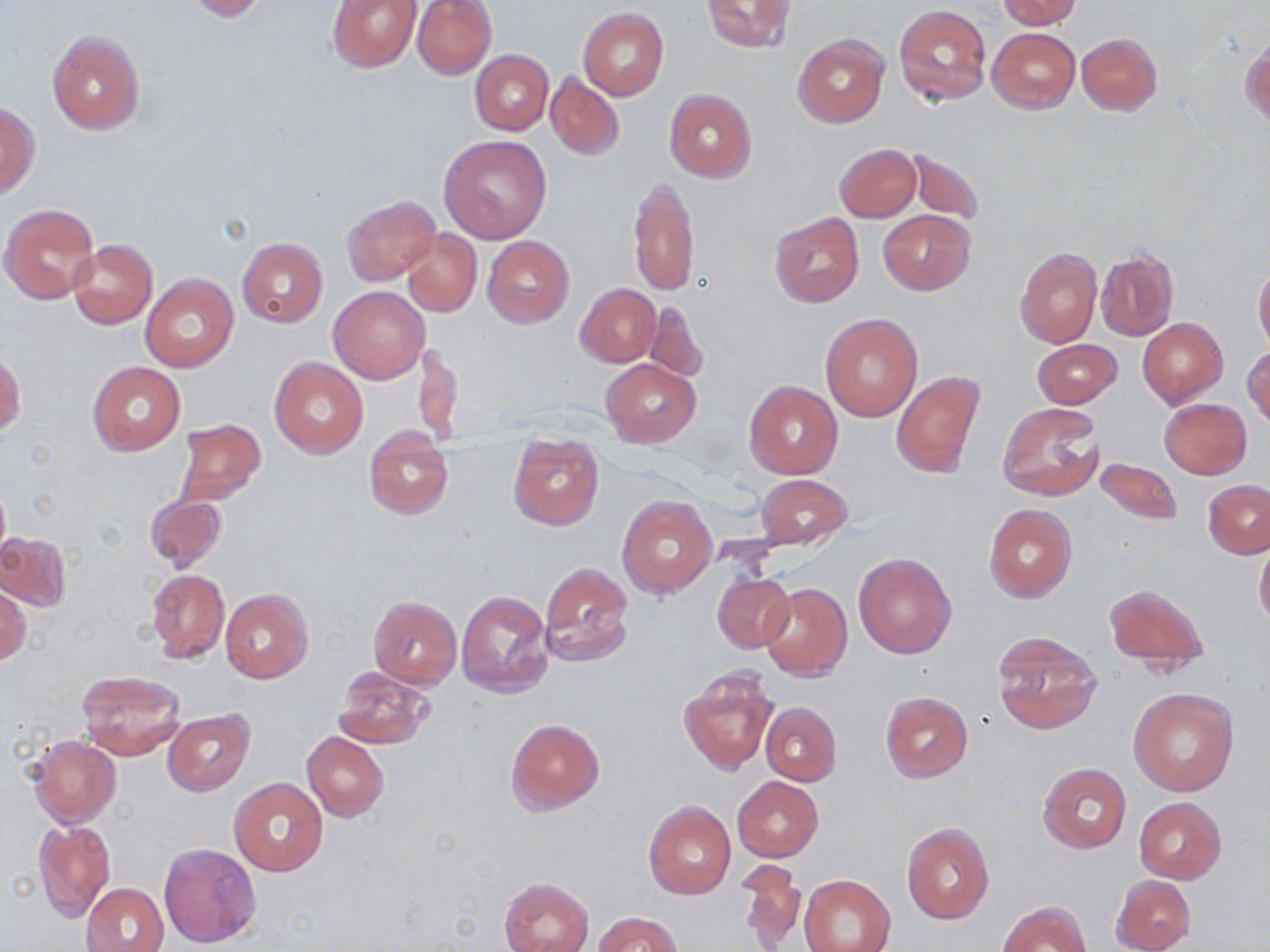

slide_level_diagnosis: negative for blood parasites
modality: optical microscopy
preparation: thin blood film
field_of_view: single
stain: May-Grünwald-Giemsa
magnification: 1000x
image_size: 1270×952 pixels
uninfected_red_blood_cell_locations: 'approximate bounding boxes as (x1, y1, x2, y2) in pixels: (182, 0, 267, 21), (328, 0, 421, 73), (412, 0, 496, 79), (998, 0, 1083, 28), (700, 1, 796, 54), (894, 5, 991, 106), (577, 8, 668, 100), (988, 27, 1080, 114), (47, 30, 144, 135), (1076, 33, 1162, 115), (1241, 34, 1269, 131), (793, 35, 888, 127), (471, 50, 552, 134), (544, 71, 624, 162), (664, 88, 757, 184), (0, 100, 38, 197), (440, 135, 552, 243), (834, 143, 921, 223), (904, 148, 985, 227), (629, 174, 700, 297), (342, 194, 441, 286), (1, 203, 99, 303), (769, 210, 865, 308), (878, 211, 975, 294), (400, 228, 482, 317), (482, 236, 574, 327), (236, 238, 328, 328), (67, 239, 158, 330), (1014, 248, 1101, 348), (1095, 249, 1180, 342), (1254, 259, 1270, 354), (141, 274, 237, 372), (575, 283, 660, 367), (329, 287, 429, 384), (643, 299, 709, 384), (821, 313, 923, 421), (1137, 317, 1227, 408), (413, 338, 464, 449), (1031, 339, 1123, 409), (1243, 345, 1270, 429), (1, 351, 24, 436), (269, 358, 368, 459), (602, 359, 700, 447), (87, 362, 185, 454), (891, 370, 985, 480), (744, 380, 842, 479), (1158, 399, 1252, 479), (996, 401, 1105, 503), (174, 419, 265, 507), (364, 426, 454, 521), (507, 434, 604, 530), (1094, 456, 1182, 525), (754, 474, 853, 551), (1203, 479, 1270, 558), (143, 494, 227, 573), (617, 494, 716, 599), (983, 503, 1077, 603), (0, 532, 72, 611), (1255, 538, 1270, 632), (854, 552, 956, 658), (539, 562, 634, 667), (147, 568, 229, 662), (711, 571, 795, 654), (1103, 582, 1211, 676), (759, 584, 852, 681), (1, 585, 31, 665), (221, 589, 313, 683), (456, 589, 553, 699), (368, 596, 462, 690), (991, 630, 1102, 735), (333, 666, 436, 750), (677, 666, 779, 776), (76, 670, 186, 760), (1128, 686, 1239, 796), (879, 690, 973, 783), (760, 702, 841, 786), (163, 711, 254, 797), (505, 718, 605, 814), (302, 731, 389, 821), (26, 735, 121, 828), (1037, 762, 1131, 853), (732, 776, 825, 862), (229, 778, 329, 878), (1133, 797, 1226, 883), (643, 800, 737, 900), (32, 820, 115, 922), (900, 822, 995, 925), (158, 843, 261, 948), (736, 862, 806, 952), (1109, 873, 1196, 952), (800, 874, 896, 952), (500, 877, 594, 952), (82, 882, 169, 952), (997, 899, 1091, 952), (595, 912, 681, 951)'